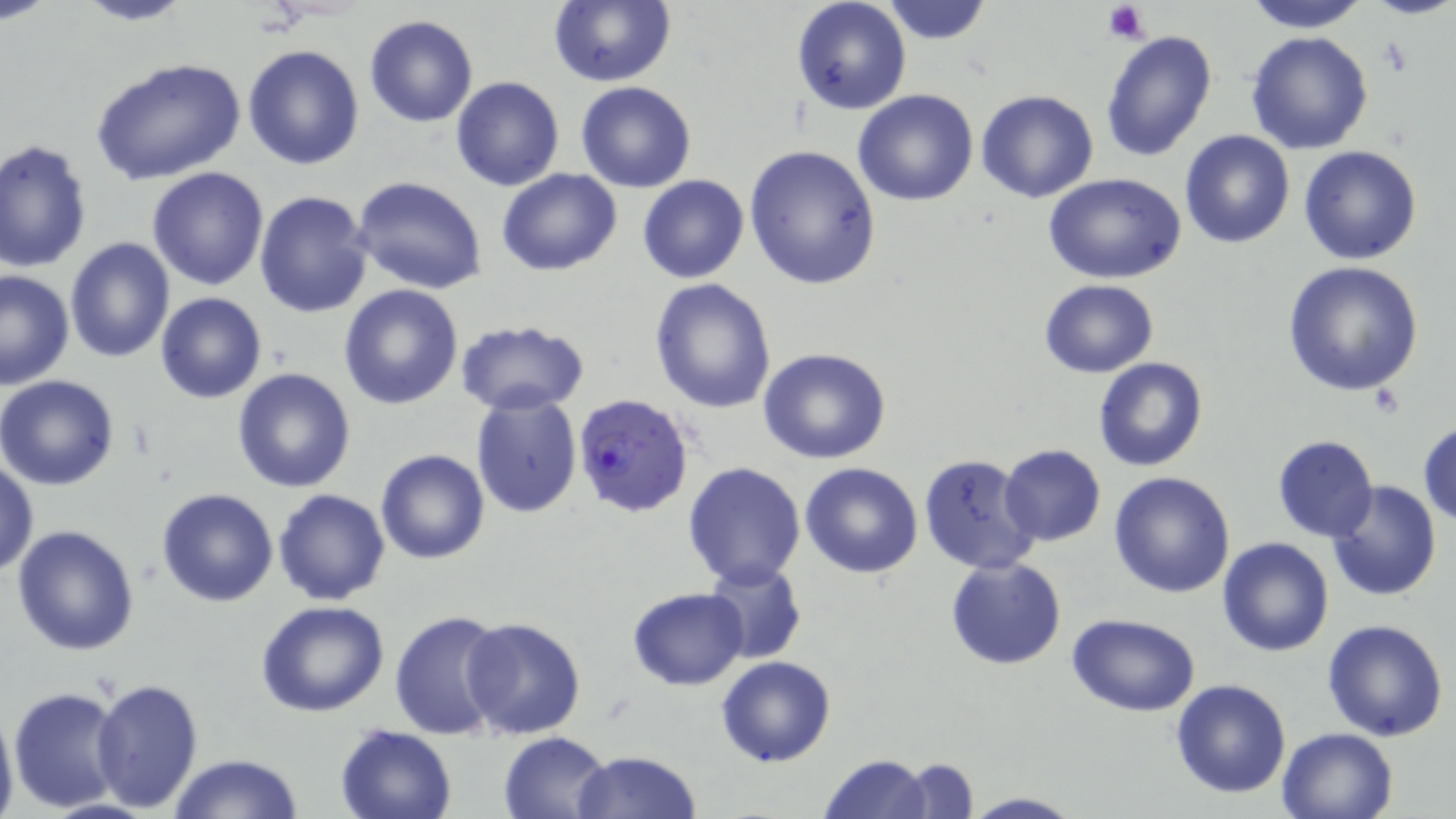

Approximate bounding boxes as (x1, y1, x2, y2) in pixels. Plasmodium falciparum-infected red blood cell locations: (573, 394, 695, 518). Platelet locations: (1103, 2, 1150, 43). Uninfected red blood cell locations: (71, 0, 197, 26), (549, 0, 675, 87), (1242, 0, 1371, 31), (1369, 0, 1454, 21), (790, 1, 912, 116), (878, 2, 997, 47), (364, 15, 479, 128), (1100, 28, 1217, 160), (1245, 31, 1374, 155), (243, 44, 364, 170), (89, 57, 246, 185), (450, 76, 563, 191), (576, 81, 697, 194), (852, 89, 979, 206), (976, 90, 1099, 204), (1179, 128, 1295, 249), (1, 139, 94, 272), (743, 143, 882, 289), (1298, 145, 1422, 264), (147, 166, 270, 291), (497, 167, 622, 276), (1044, 172, 1187, 284), (637, 174, 748, 283), (353, 176, 487, 294), (254, 189, 374, 318), (63, 236, 175, 363), (1281, 261, 1426, 398), (0, 270, 73, 389), (650, 277, 777, 413), (1039, 279, 1159, 376), (338, 285, 464, 410), (155, 292, 266, 403), (455, 320, 588, 417), (759, 347, 890, 464), (1093, 356, 1208, 471), (232, 367, 356, 492), (0, 375, 120, 491), (469, 391, 582, 519), (1418, 420, 1456, 527), (1272, 435, 1379, 542), (998, 445, 1105, 546), (376, 449, 489, 564), (916, 451, 1041, 575), (0, 457, 38, 578), (682, 462, 807, 588), (800, 463, 923, 580), (1109, 471, 1235, 596), (1327, 480, 1442, 602), (273, 488, 390, 605), (156, 489, 279, 607), (10, 524, 140, 657), (1217, 537, 1334, 656), (945, 557, 1067, 671), (702, 559, 807, 665), (627, 588, 749, 690), (255, 601, 389, 718), (388, 609, 509, 739), (1066, 612, 1201, 717), (460, 615, 586, 739), (1322, 618, 1449, 741), (716, 654, 836, 767), (92, 676, 204, 814), (1170, 679, 1292, 799), (9, 684, 128, 812), (0, 705, 18, 819), (334, 724, 458, 819), (1276, 726, 1398, 819), (499, 732, 613, 819), (573, 750, 701, 819), (171, 753, 303, 819), (817, 754, 933, 819), (898, 758, 978, 818), (961, 792, 1083, 819). Slide-level diagnosis: Plasmodium falciparum. Captured at 1000x magnification. Optical microscopy. Image is 1456×819 pixels. May-Grünwald-Giemsa-stained preparation. Thin blood film. Single field of view.